Locate every Plasmodium ovale-infected red blood cell.
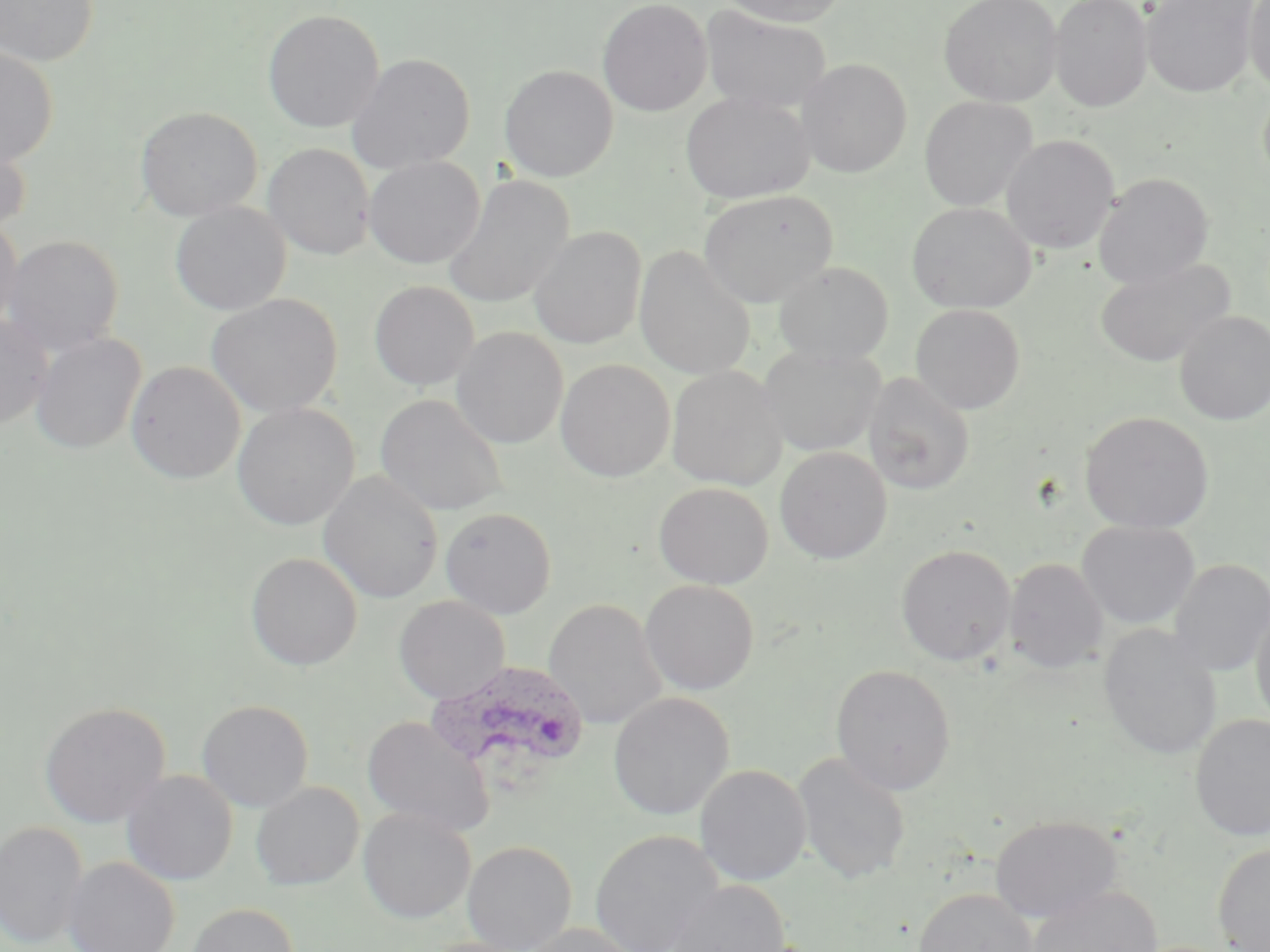

Approximate bounding boxes as named x1/y1/x2/y2 corners in pixels.
Plasmodium ovale-infected red blood cells: (x1=427, y1=661, x2=590, y2=785).

slide_level_diagnosis: Plasmodium ovale
modality: light microscopy
preparation: thin blood smear
magnification: 1000x
stain: May-Grünwald-Giemsa
field_of_view: one of a larger specimen
uninfected_red_blood_cell_locations: 'approximate bounding boxes as named x1/y1/x2/y2 corners in pixels: (x1=0, y1=0, x2=99, y2=68), (x1=597, y1=0, x2=712, y2=117), (x1=718, y1=0, x2=849, y2=27), (x1=939, y1=0, x2=1063, y2=107), (x1=1049, y1=0, x2=1153, y2=112), (x1=1142, y1=0, x2=1261, y2=98), (x1=1244, y1=0, x2=1270, y2=96), (x1=699, y1=6, x2=832, y2=115), (x1=262, y1=9, x2=385, y2=133), (x1=0, y1=46, x2=59, y2=167), (x1=347, y1=53, x2=475, y2=174), (x1=797, y1=58, x2=913, y2=177), (x1=499, y1=64, x2=618, y2=182), (x1=1258, y1=85, x2=1270, y2=191), (x1=680, y1=92, x2=815, y2=205), (x1=919, y1=96, x2=1038, y2=212), (x1=135, y1=106, x2=262, y2=221), (x1=0, y1=132, x2=32, y2=234), (x1=1001, y1=135, x2=1119, y2=254), (x1=263, y1=143, x2=375, y2=260), (x1=364, y1=156, x2=484, y2=269), (x1=1093, y1=172, x2=1214, y2=288), (x1=442, y1=174, x2=574, y2=309), (x1=698, y1=189, x2=837, y2=307), (x1=907, y1=201, x2=1037, y2=313), (x1=170, y1=202, x2=291, y2=315), (x1=0, y1=219, x2=23, y2=331), (x1=529, y1=225, x2=646, y2=350), (x1=2, y1=235, x2=124, y2=356), (x1=634, y1=245, x2=756, y2=380), (x1=1095, y1=258, x2=1234, y2=368), (x1=773, y1=261, x2=893, y2=367), (x1=369, y1=281, x2=479, y2=391), (x1=206, y1=293, x2=343, y2=418), (x1=910, y1=303, x2=1026, y2=414), (x1=1174, y1=311, x2=1270, y2=425), (x1=0, y1=314, x2=53, y2=430), (x1=451, y1=327, x2=568, y2=449), (x1=30, y1=333, x2=147, y2=454), (x1=758, y1=345, x2=884, y2=457), (x1=555, y1=359, x2=675, y2=481), (x1=126, y1=361, x2=245, y2=484), (x1=666, y1=366, x2=787, y2=490), (x1=863, y1=372, x2=975, y2=495), (x1=374, y1=393, x2=509, y2=517), (x1=232, y1=402, x2=359, y2=530), (x1=1079, y1=410, x2=1214, y2=534), (x1=775, y1=446, x2=892, y2=564), (x1=318, y1=471, x2=443, y2=604), (x1=653, y1=481, x2=774, y2=589), (x1=440, y1=507, x2=557, y2=619), (x1=1077, y1=520, x2=1200, y2=630), (x1=896, y1=544, x2=1016, y2=667), (x1=245, y1=552, x2=363, y2=670), (x1=1004, y1=557, x2=1108, y2=673), (x1=1168, y1=559, x2=1270, y2=677), (x1=639, y1=579, x2=759, y2=695), (x1=393, y1=595, x2=511, y2=704), (x1=1250, y1=597, x2=1270, y2=730), (x1=543, y1=599, x2=668, y2=730), (x1=1098, y1=624, x2=1222, y2=761), (x1=831, y1=664, x2=956, y2=795), (x1=608, y1=692, x2=734, y2=821), (x1=196, y1=699, x2=314, y2=812), (x1=39, y1=701, x2=170, y2=828), (x1=1189, y1=714, x2=1270, y2=842), (x1=362, y1=715, x2=495, y2=837), (x1=792, y1=751, x2=911, y2=886), (x1=694, y1=764, x2=811, y2=886), (x1=121, y1=770, x2=238, y2=886), (x1=251, y1=782, x2=364, y2=890), (x1=358, y1=807, x2=476, y2=923), (x1=990, y1=815, x2=1122, y2=922), (x1=0, y1=821, x2=89, y2=949), (x1=590, y1=829, x2=724, y2=952), (x1=462, y1=840, x2=577, y2=951), (x1=1212, y1=842, x2=1270, y2=952), (x1=63, y1=857, x2=179, y2=952), (x1=664, y1=880, x2=791, y2=952), (x1=1026, y1=885, x2=1163, y2=952), (x1=914, y1=888, x2=1038, y2=952), (x1=186, y1=902, x2=299, y2=952), (x1=519, y1=923, x2=645, y2=952)'
image_size: 1270×952 pixels